Assess the morphology of the red blood cells.
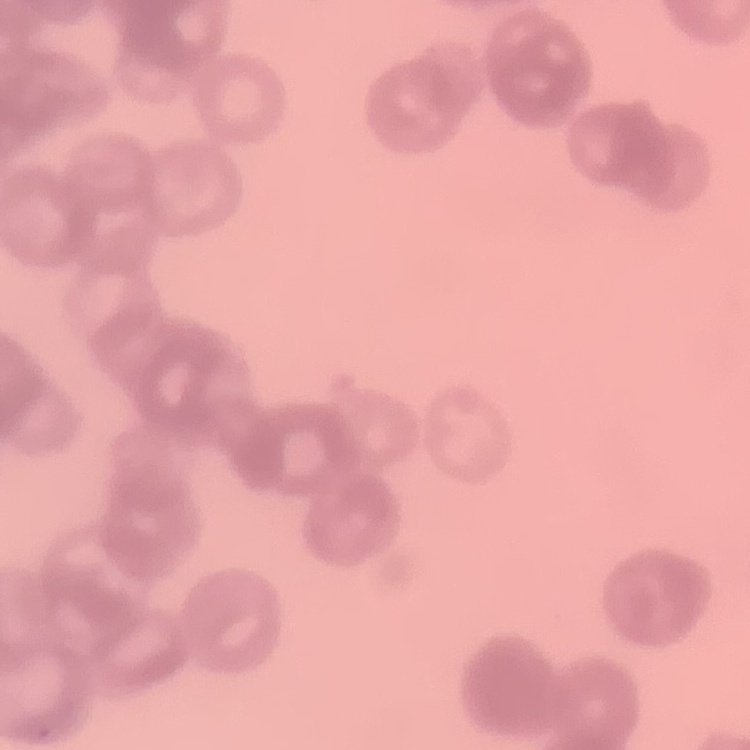

They show rouleaux formation.

Thin peripheral smear. Stained with either Field's or Giemsa. One tile cut from a larger photomicrograph.